Identify the cell.
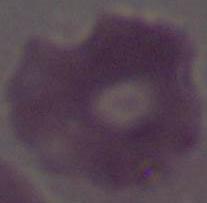
This is an erythrocyte.

1000x magnification. Photomicrograph.